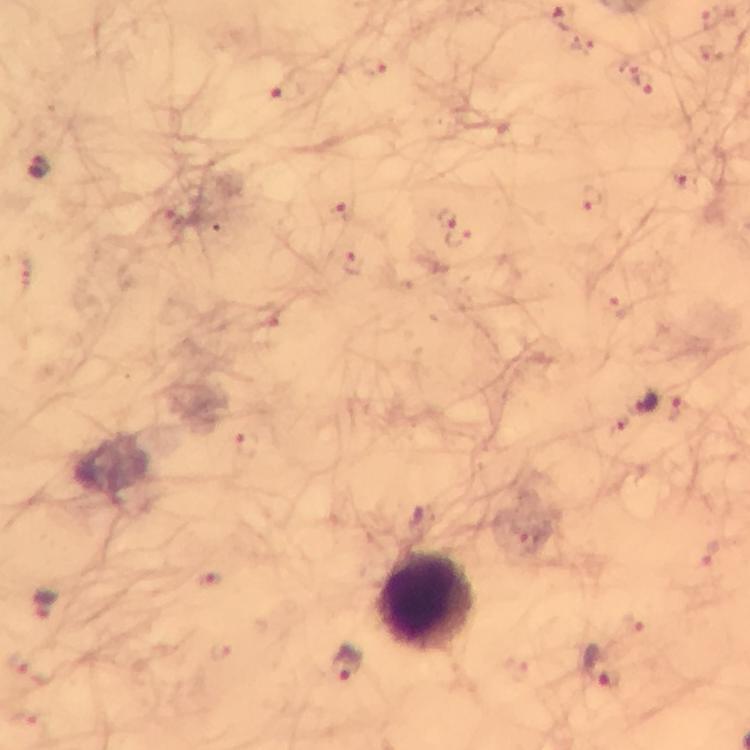
Approximate object centers, in pixels from the top-left corner. Plasmodium parasite locations: (x=714, y=17), (x=373, y=70), (x=642, y=80), (x=288, y=91), (x=38, y=168), (x=685, y=178), (x=593, y=198), (x=340, y=209), (x=162, y=217), (x=445, y=218), (x=459, y=236), (x=354, y=264), (x=620, y=307), (x=645, y=402), (x=678, y=407), (x=247, y=446), (x=531, y=541), (x=710, y=553), (x=210, y=580), (x=48, y=604), (x=633, y=623), (x=221, y=649), (x=348, y=665), (x=597, y=666), (x=29, y=668), (x=25, y=718). Leukocyte locations: (x=427, y=601). Giemsa-stained preparation. Thick smear. Image is 750×750 pixels. Cropped region of a single field of view. Immersion oil applied. 100x magnification. From a malaria diagnostic workup. Photographed with a smartphone mounted on the microscope.